Give the position of every malaria parasite.
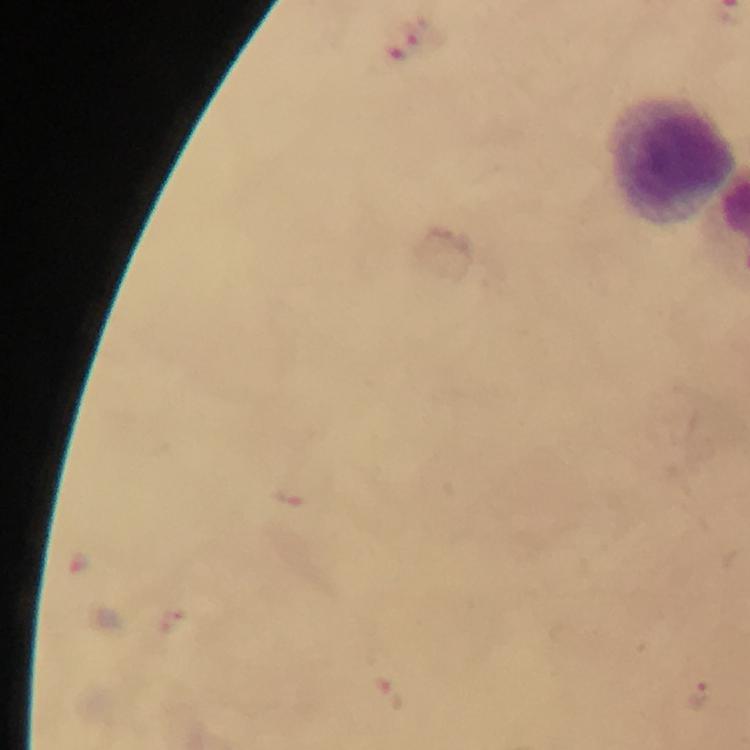
Approximate centers as (x, y) in pixels.
Malaria parasites: (413, 36), (78, 565), (388, 695), (698, 696).

{
  "context": "from a diagnostic examination for malaria",
  "preparation": "thick blood film",
  "leukocyte_locations": "approximate centers as (x, y) in pixels: (671, 162)",
  "magnification": "100x",
  "cropped_from": "one field of view",
  "capture": "smartphone mounted on the microscope",
  "stain": "Giemsa",
  "image_size": "750×750 pixels",
  "immersion_oil": "applied"
}